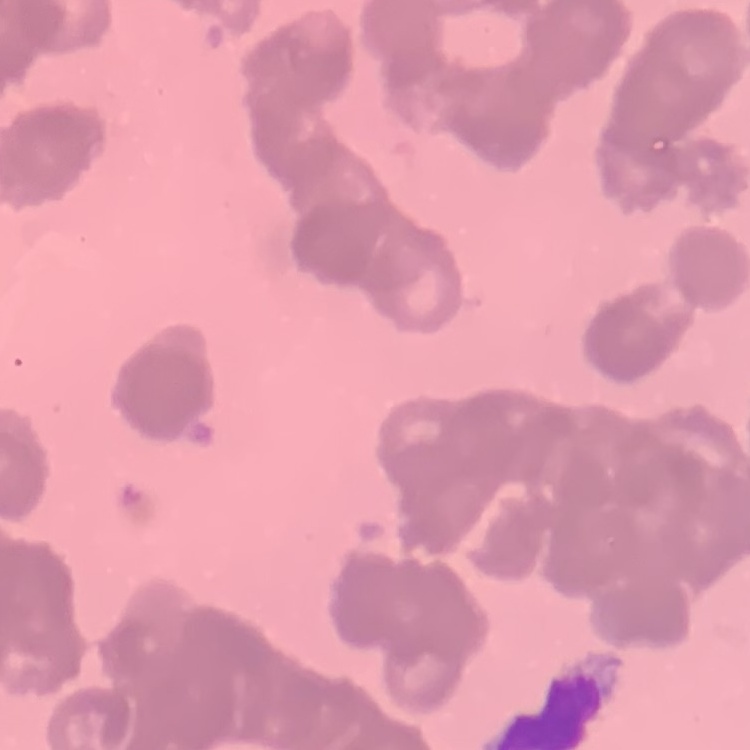
The erythrocytes exhibit rouleaux formation. Stained with either Field's or Giemsa. One tile cut from a larger photomicrograph. Thin blood smear.